Name the cell type shown.
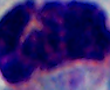
A leukocyte.

Summary:
  - Modality: micrograph
  - Magnification: 1000x